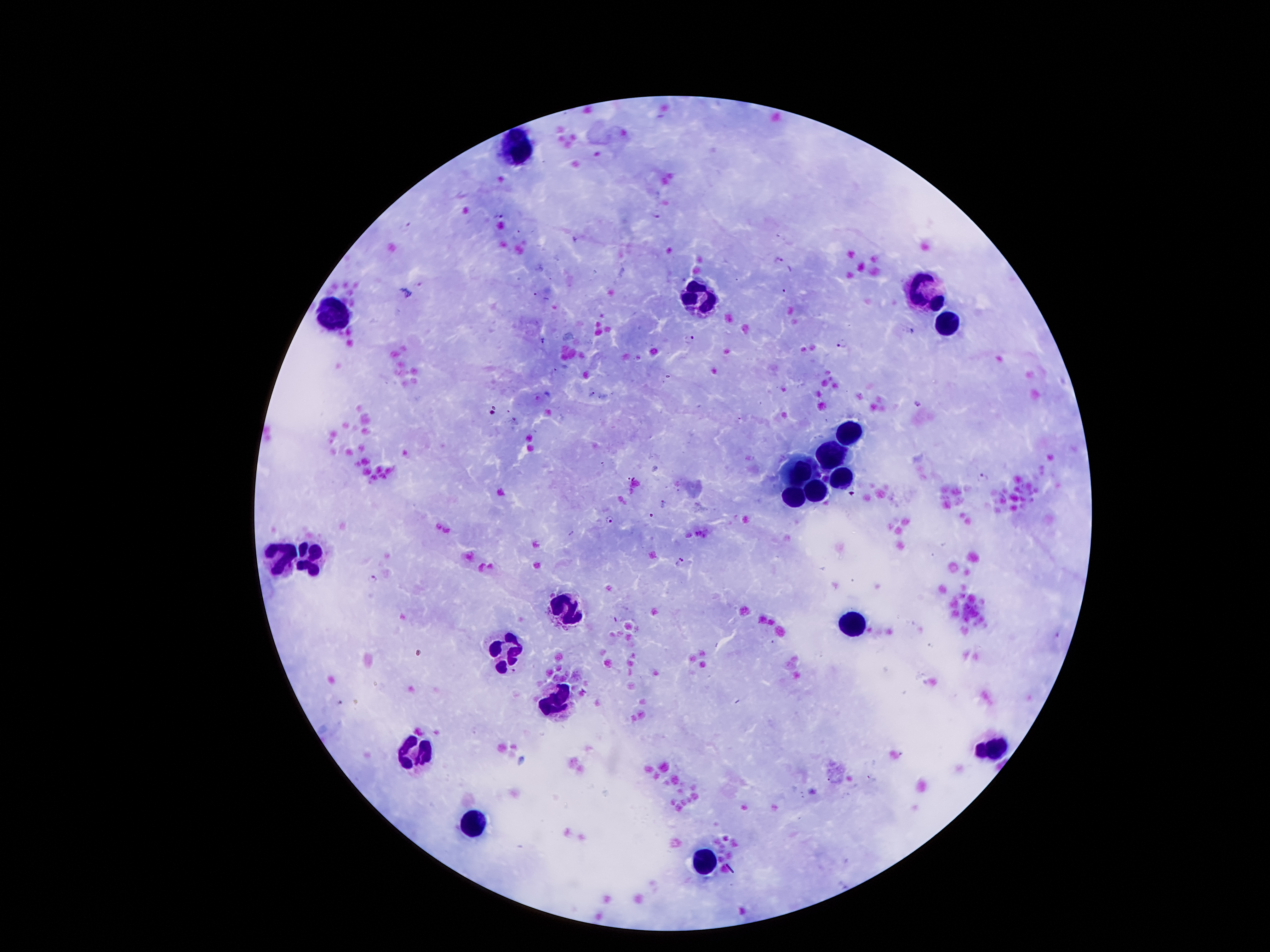

Approximate centers as [x, y] in pixels. Plasmodium parasite locations: [657, 214], [499, 216], [407, 225], [777, 259], [419, 286], [786, 289], [688, 338], [843, 344], [918, 404], [492, 413], [984, 477], [663, 503], [608, 518], [679, 562], [373, 579], [869, 777]. Leukocyte locations: [516, 148], [932, 287], [702, 299], [325, 315], [946, 324], [850, 435], [834, 455], [801, 477], [840, 480], [813, 490], [795, 496], [311, 556], [276, 558], [563, 606], [856, 621], [512, 653], [553, 699], [993, 749], [417, 752], [473, 824], [704, 862]. 100x magnification. Thick blood film. Patient malaria status: infected with Plasmodium falciparum. Smartphone photograph taken through the microscope eyepiece. Giemsa-stained preparation. Image is 1270×952 pixels. One field from this slide.